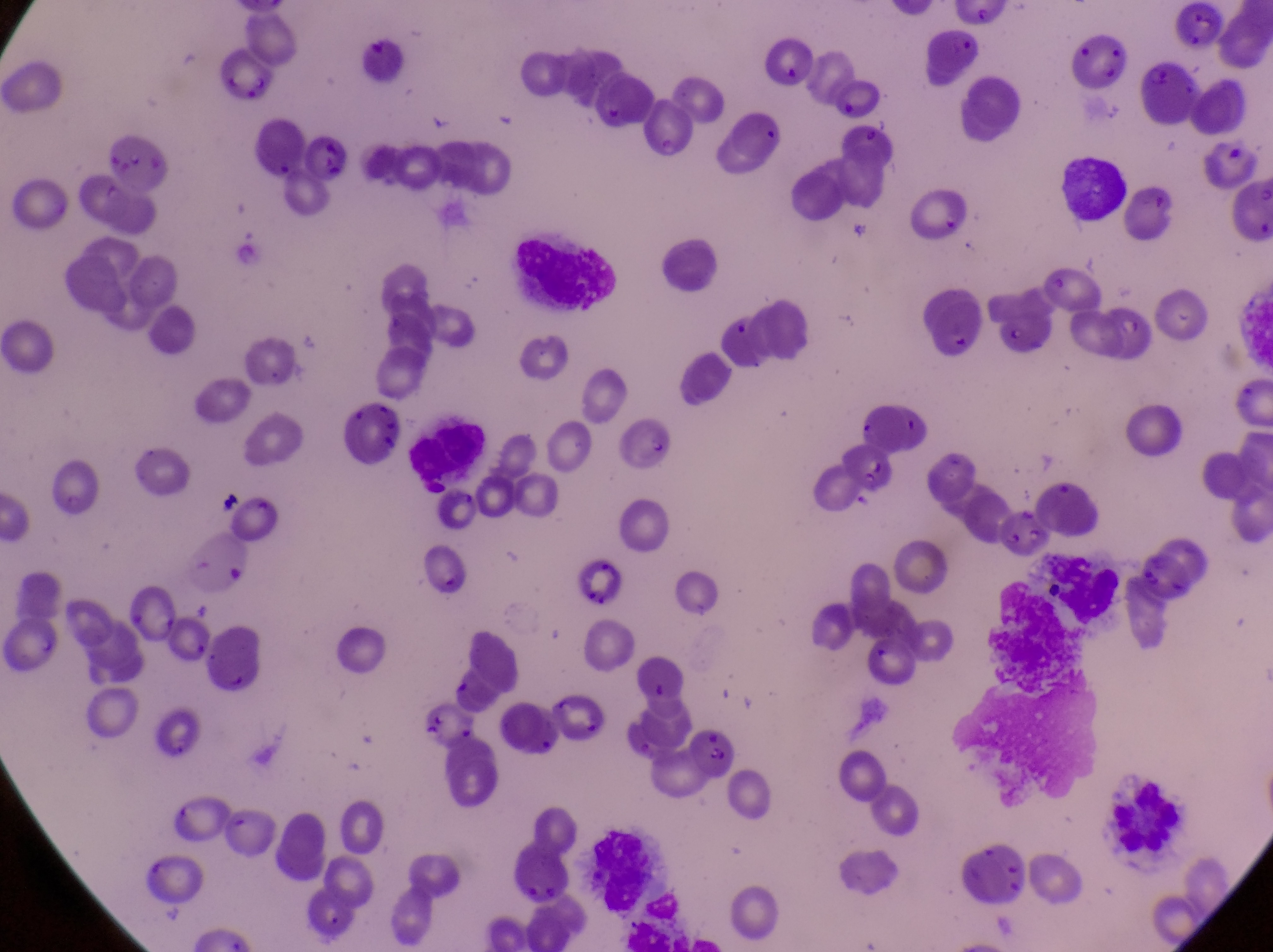
Approximate bounding boxes as [left, top, right, bottom] in pixels. Parasitised red blood cell locations: [612, 420, 677, 477], [419, 544, 491, 616], [1133, 556, 1202, 608], [681, 721, 741, 795]. Leukocyte locations: [1055, 148, 1130, 225], [512, 225, 624, 315], [1028, 545, 1125, 628]. Artifact (platelet-like body, stain precipitate, or debris) locations: [213, 491, 245, 519]. Image is 1273×952 pixels. Thin blood smear. Captured by a smartphone held over the eyepiece of an Olympus CX-23 microscope. Magnification of 1000x. One field of view. Collected in Uganda.